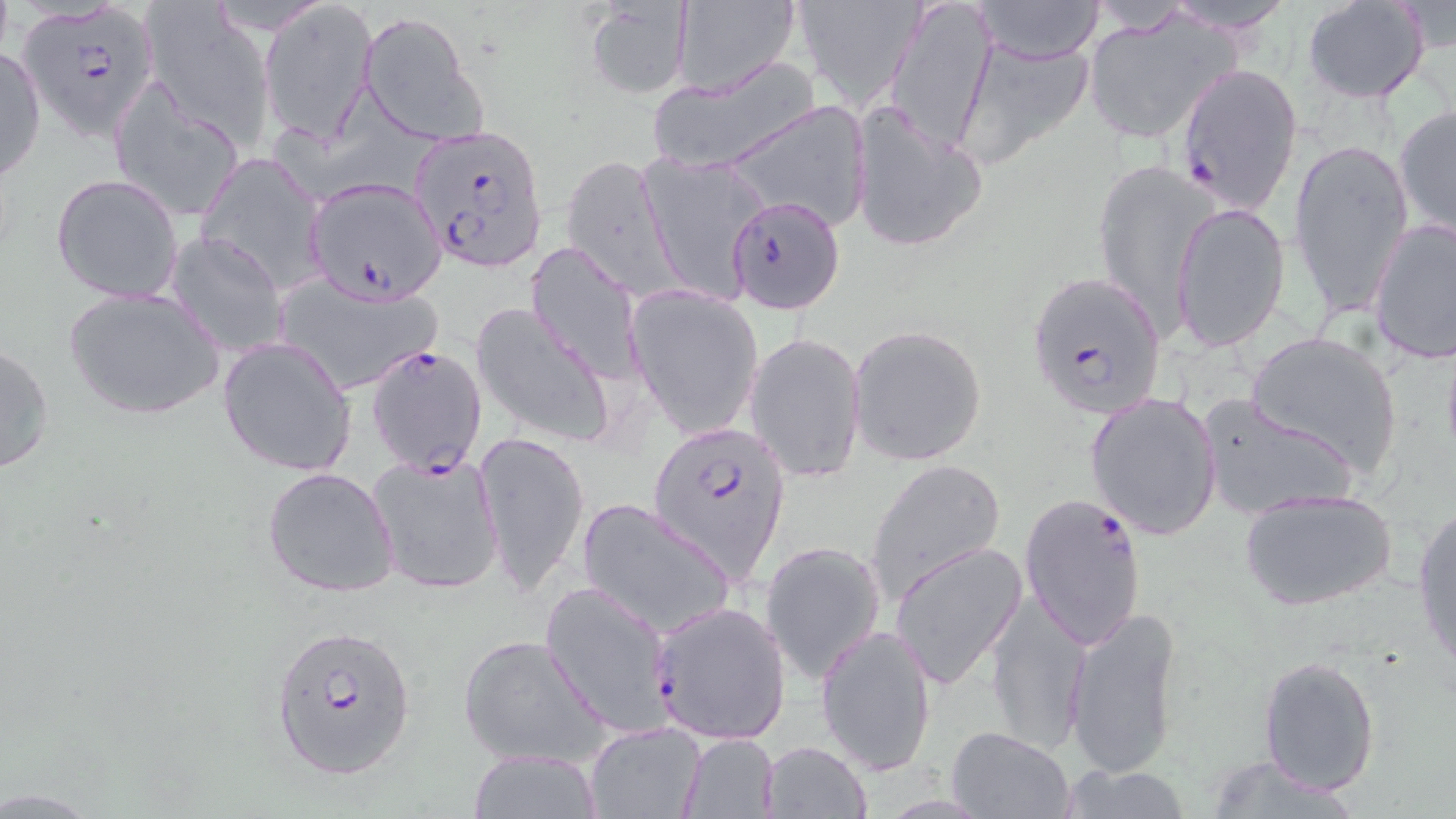
slide_level_diagnosis: Plasmodium falciparum
magnification: 1000x
field_of_view: single
uninfected_red_blood_cell_locations: 'approximate bounding boxes as named x1/y1/x2/y2 corners in pixels: (x1=261, y1=0, x2=378, y2=145), (x1=583, y1=0, x2=693, y2=98), (x1=672, y1=0, x2=801, y2=97), (x1=788, y1=0, x2=925, y2=106), (x1=885, y1=0, x2=996, y2=156), (x1=970, y1=0, x2=1106, y2=65), (x1=1154, y1=0, x2=1300, y2=34), (x1=1303, y1=1, x2=1431, y2=104), (x1=140, y1=2, x2=276, y2=148), (x1=1083, y1=8, x2=1238, y2=145), (x1=358, y1=12, x2=482, y2=142), (x1=955, y1=32, x2=1097, y2=165), (x1=0, y1=45, x2=46, y2=184), (x1=649, y1=56, x2=819, y2=179), (x1=108, y1=77, x2=248, y2=222), (x1=722, y1=99, x2=874, y2=233), (x1=850, y1=102, x2=987, y2=253), (x1=1393, y1=104, x2=1455, y2=241), (x1=1287, y1=136, x2=1415, y2=319), (x1=197, y1=152, x2=327, y2=293), (x1=640, y1=152, x2=769, y2=303), (x1=562, y1=155, x2=678, y2=298), (x1=1090, y1=156, x2=1216, y2=329), (x1=51, y1=174, x2=184, y2=304), (x1=1171, y1=203, x2=1291, y2=351), (x1=1368, y1=217, x2=1456, y2=364), (x1=166, y1=229, x2=286, y2=356), (x1=524, y1=241, x2=646, y2=386), (x1=269, y1=270, x2=443, y2=395), (x1=63, y1=286, x2=225, y2=420), (x1=627, y1=286, x2=764, y2=440), (x1=471, y1=302, x2=615, y2=446), (x1=848, y1=324, x2=989, y2=467), (x1=1245, y1=330, x2=1403, y2=476), (x1=746, y1=332, x2=868, y2=483), (x1=217, y1=335, x2=356, y2=476), (x1=0, y1=340, x2=54, y2=479), (x1=1085, y1=390, x2=1224, y2=541), (x1=1196, y1=393, x2=1358, y2=520), (x1=477, y1=428, x2=589, y2=600), (x1=366, y1=452, x2=506, y2=596), (x1=865, y1=458, x2=1005, y2=600), (x1=262, y1=467, x2=402, y2=599), (x1=1238, y1=485, x2=1399, y2=612), (x1=577, y1=496, x2=735, y2=639), (x1=1412, y1=504, x2=1456, y2=675), (x1=761, y1=540, x2=888, y2=686), (x1=888, y1=541, x2=1027, y2=691), (x1=985, y1=591, x2=1090, y2=755), (x1=649, y1=600, x2=791, y2=744), (x1=1063, y1=605, x2=1185, y2=782), (x1=815, y1=624, x2=937, y2=776), (x1=457, y1=633, x2=610, y2=770), (x1=1259, y1=655, x2=1380, y2=794), (x1=584, y1=721, x2=706, y2=817), (x1=946, y1=725, x2=1076, y2=818), (x1=677, y1=734, x2=780, y2=819), (x1=758, y1=740, x2=871, y2=819), (x1=466, y1=750, x2=603, y2=819), (x1=1203, y1=755, x2=1367, y2=817), (x1=1054, y1=765, x2=1197, y2=818)'
image_size: 1456×819 pixels
modality: optical microscopy
stain: May-Grünwald-Giemsa
preparation: thin blood film
plasmodium_falciparum_infected_red_blood_cell_locations: 'approximate bounding boxes as named x1/y1/x2/y2 corners in pixels: (x1=17, y1=3, x2=159, y2=139), (x1=1176, y1=61, x2=1304, y2=215), (x1=409, y1=124, x2=548, y2=272), (x1=304, y1=179, x2=445, y2=303), (x1=727, y1=196, x2=846, y2=316), (x1=1028, y1=270, x2=1167, y2=419), (x1=368, y1=343, x2=488, y2=478), (x1=648, y1=419, x2=791, y2=591), (x1=1019, y1=489, x2=1148, y2=650), (x1=540, y1=579, x2=676, y2=739), (x1=271, y1=622, x2=417, y2=781)'